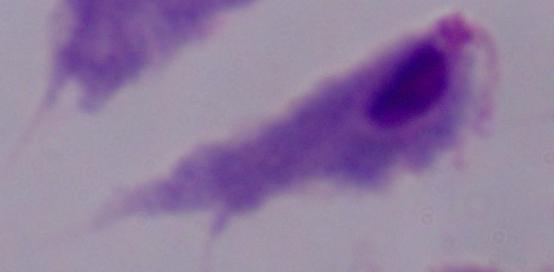

identification = trichomonad
modality = micrograph
magnification = 1000x